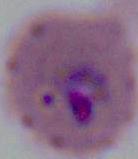

Photomicrograph. A Plasmodium parasite is shown. Captured at either 400x or 1000x magnification.